Classify this cell by malaria status.
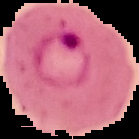
Parasitized.

{
  "image_type": "segmented cell region on a black background",
  "image_size": "139×139 pixels",
  "preparation": "thin blood smear"
}